Name the cell type shown.
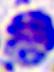
A leukocyte.

Micrograph. 400x magnification.